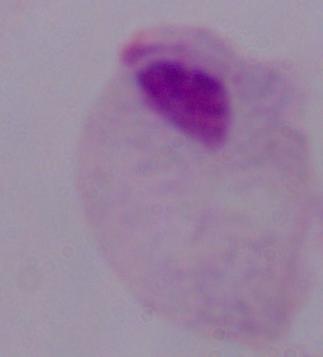
Summary:
  - Magnification: 1000x
  - Modality: micrograph
  - Identification: trichomonad